Give the extent of all Plasmodium vivax-infected red blood cells.
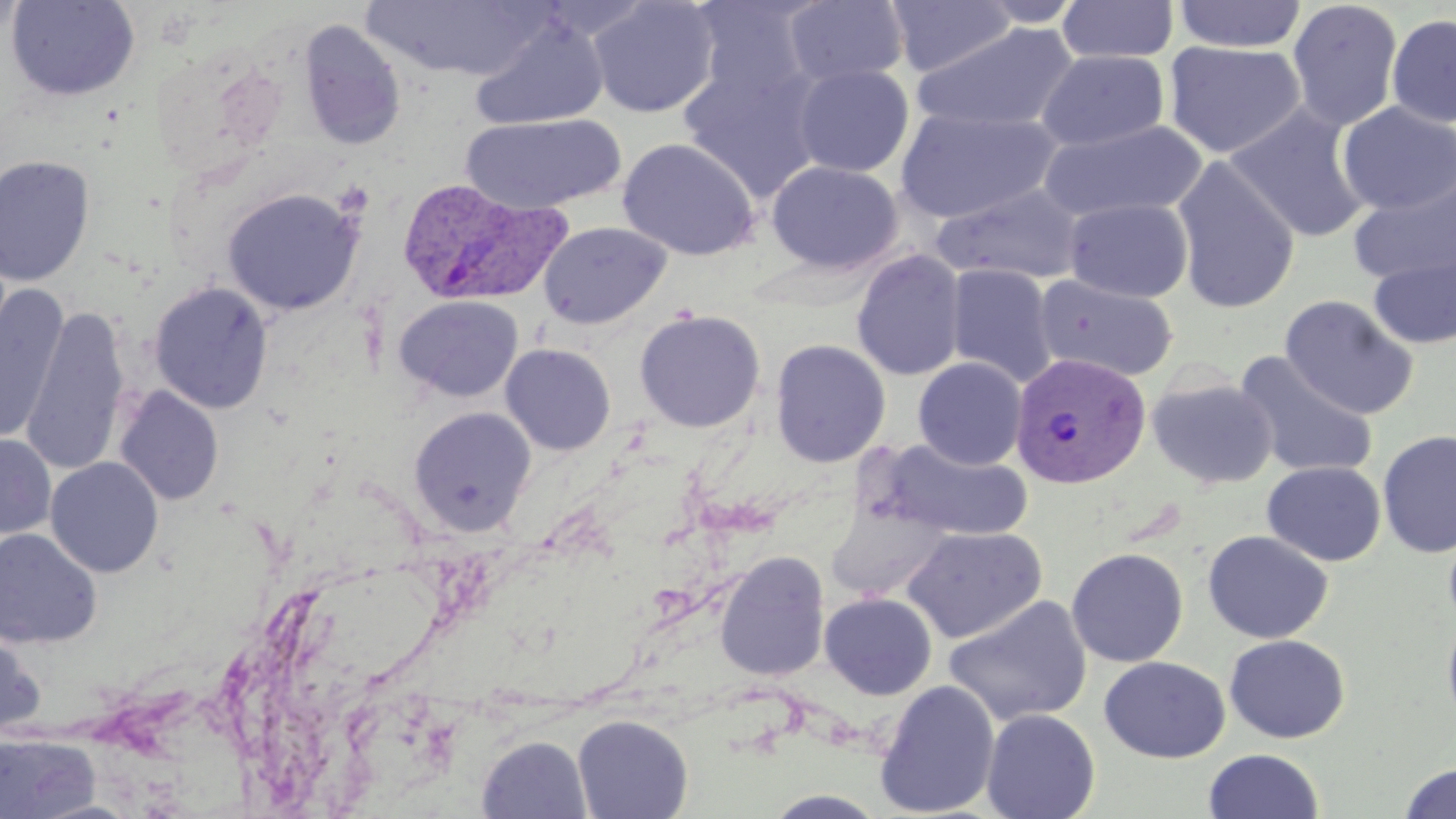
Approximate bounding boxes as [x1, y1, x2, y2] in pixels.
Plasmodium vivax-infected red blood cells: [396, 178, 570, 307], [1009, 352, 1151, 490].

slide-level diagnosis = Plasmodium vivax
image size = 1456×819 pixels
uninfected red blood cell locations = approximate bounding boxes as [x1, y1, x2, y2] in pixels: [586, 0, 721, 118], [1173, 0, 1308, 53], [0, 1, 27, 48], [5, 1, 141, 101], [359, 1, 551, 81], [686, 1, 820, 109], [783, 1, 910, 87], [886, 1, 1017, 77], [976, 1, 1085, 27], [1056, 1, 1179, 63], [1287, 1, 1403, 130], [1386, 14, 1456, 127], [470, 15, 609, 132], [297, 18, 406, 150], [910, 22, 1080, 134], [1163, 40, 1306, 159], [1036, 49, 1170, 152], [679, 62, 828, 202], [792, 64, 914, 177], [1337, 102, 1456, 216], [1224, 104, 1372, 244], [894, 108, 1062, 224], [461, 114, 625, 214], [1038, 119, 1208, 223], [617, 137, 760, 261], [0, 155, 96, 287], [1171, 156, 1301, 313], [766, 161, 903, 274], [1349, 174, 1455, 287], [932, 183, 1087, 285], [222, 187, 364, 316], [1064, 197, 1194, 302], [538, 221, 671, 330], [1368, 248, 1456, 350], [851, 249, 967, 382], [944, 263, 1058, 387], [1034, 274, 1179, 383], [150, 282, 273, 414], [1, 288, 69, 444], [393, 295, 523, 402], [1279, 295, 1419, 420], [21, 307, 131, 477], [634, 308, 766, 433], [770, 339, 891, 468], [500, 343, 616, 455], [1233, 351, 1379, 481], [913, 357, 1028, 470], [1146, 375, 1279, 490], [114, 386, 224, 506], [408, 406, 536, 537], [1377, 430, 1456, 559], [0, 433, 56, 539], [881, 440, 1033, 542], [45, 457, 164, 577], [1262, 461, 1386, 566], [825, 502, 950, 602], [1443, 523, 1456, 635], [901, 525, 1047, 643], [0, 528, 102, 648], [1202, 530, 1334, 644], [1066, 547, 1188, 668], [714, 551, 830, 681], [820, 592, 937, 699], [943, 595, 1093, 726], [1442, 609, 1456, 733], [0, 627, 46, 741], [1224, 634, 1350, 743], [1099, 656, 1230, 763], [874, 680, 1001, 818], [981, 708, 1100, 819], [572, 714, 693, 819], [0, 731, 101, 819], [476, 735, 592, 818], [1202, 749, 1325, 819], [1397, 762, 1456, 819], [761, 789, 891, 818]
preparation = thin blood film
field of view = single
modality = optical microscopy
magnification = 1000x
stain = May-Grünwald-Giemsa
platelet locations = approximate bounding boxes as [x1, y1, x2, y2] in pixels: [333, 181, 373, 219]